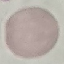
Result: no malaria parasites detected. Automatically extracted cell patch, resized to 64 × 64 pixels. Thin smear of blood. Acquired by smartphone through the microscope eyepiece. Giemsa-stained preparation.